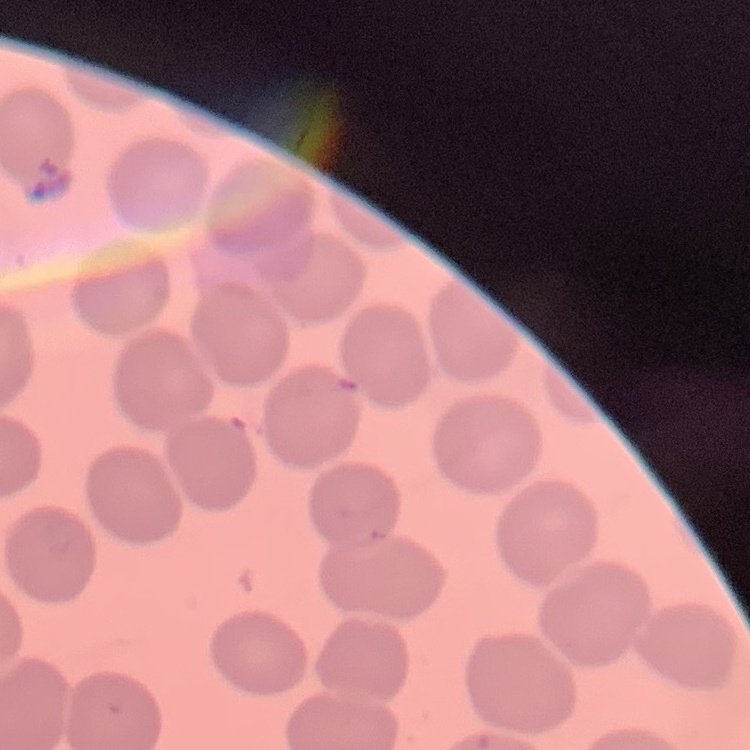
Summary:
  - Erythrocyte morphology: no rouleaux formation
  - Image type: square crop of a larger photomicrograph
  - Preparation: thin blood smear
  - Stain: Field's or Giemsa